Name the parasite shown.
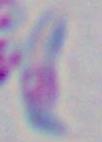
Toxoplasma gondii.

Summary:
  - Magnification: 1000x
  - Modality: photomicrograph